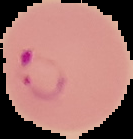

image type = segmented cell region with the area outside set to black
result = Plasmodium parasites detected
image size = 133×139 pixels
preparation = thin blood film